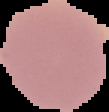
Summary:
  - Preparation: thin blood smear
  - Image size: 109×112 pixels
  - Image type: cell region segmented out of the field of view; surrounding area masked to black
  - Malaria status: uninfected